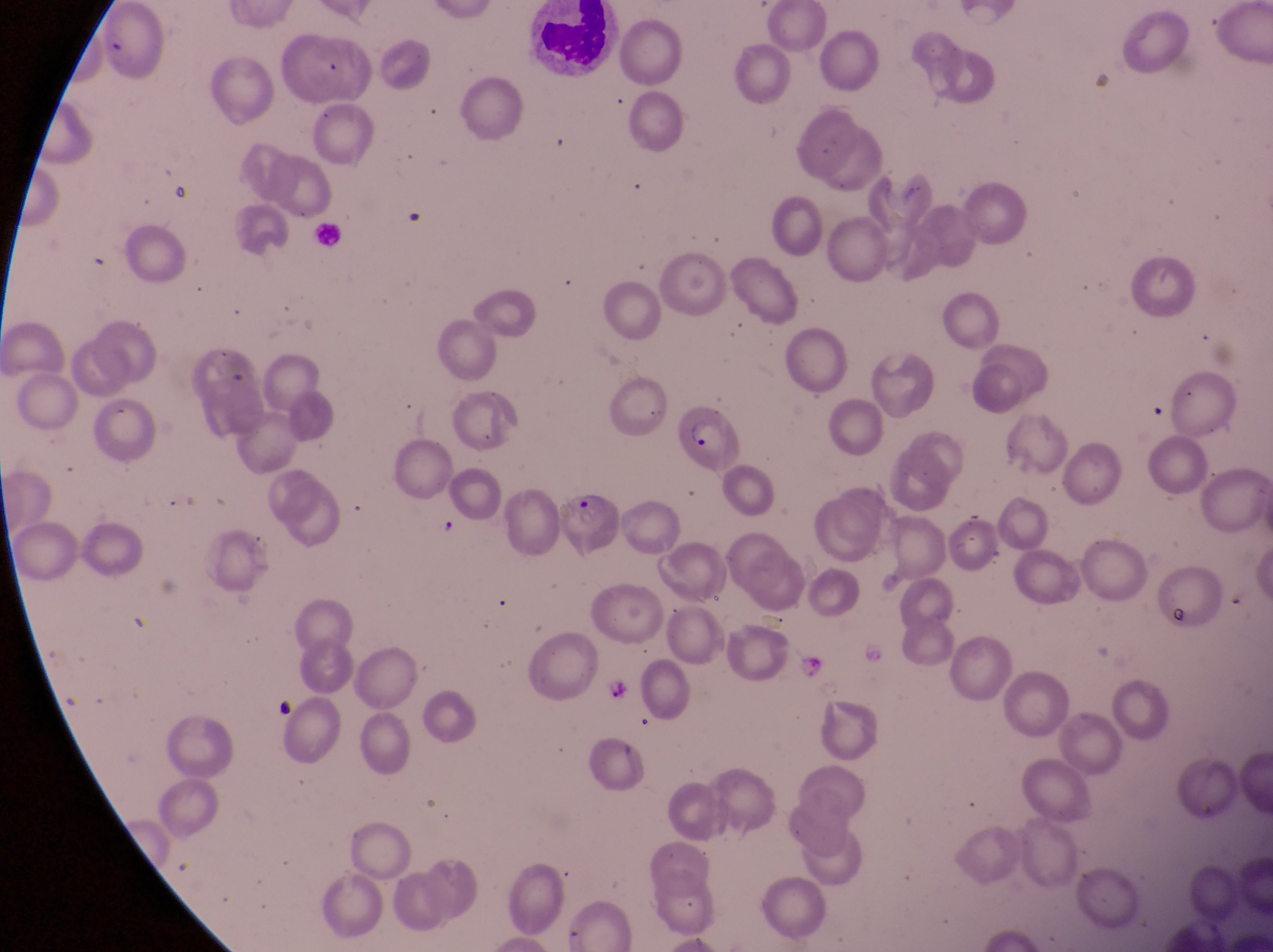

preparation = thin blood smear
image size = 1273×952 pixels
parasitised red blood cell locations = approximate bounding boxes as {left, top, right, bottom} in pixels: {679, 414, 739, 476}, {562, 489, 614, 556}
trophozoite locations = approximate bounding boxes as {left, top, right, bottom} in pixels: {796, 651, 823, 681}, {607, 677, 635, 709}
country = Uganda
magnification = 1000x
leukocyte locations = approximate bounding boxes as {left, top, right, bottom} in pixels: {522, 2, 622, 89}, {309, 220, 351, 254}
capture = smartphone photograph through the eyepiece of an Olympus CX-23 microscope
field of view = single